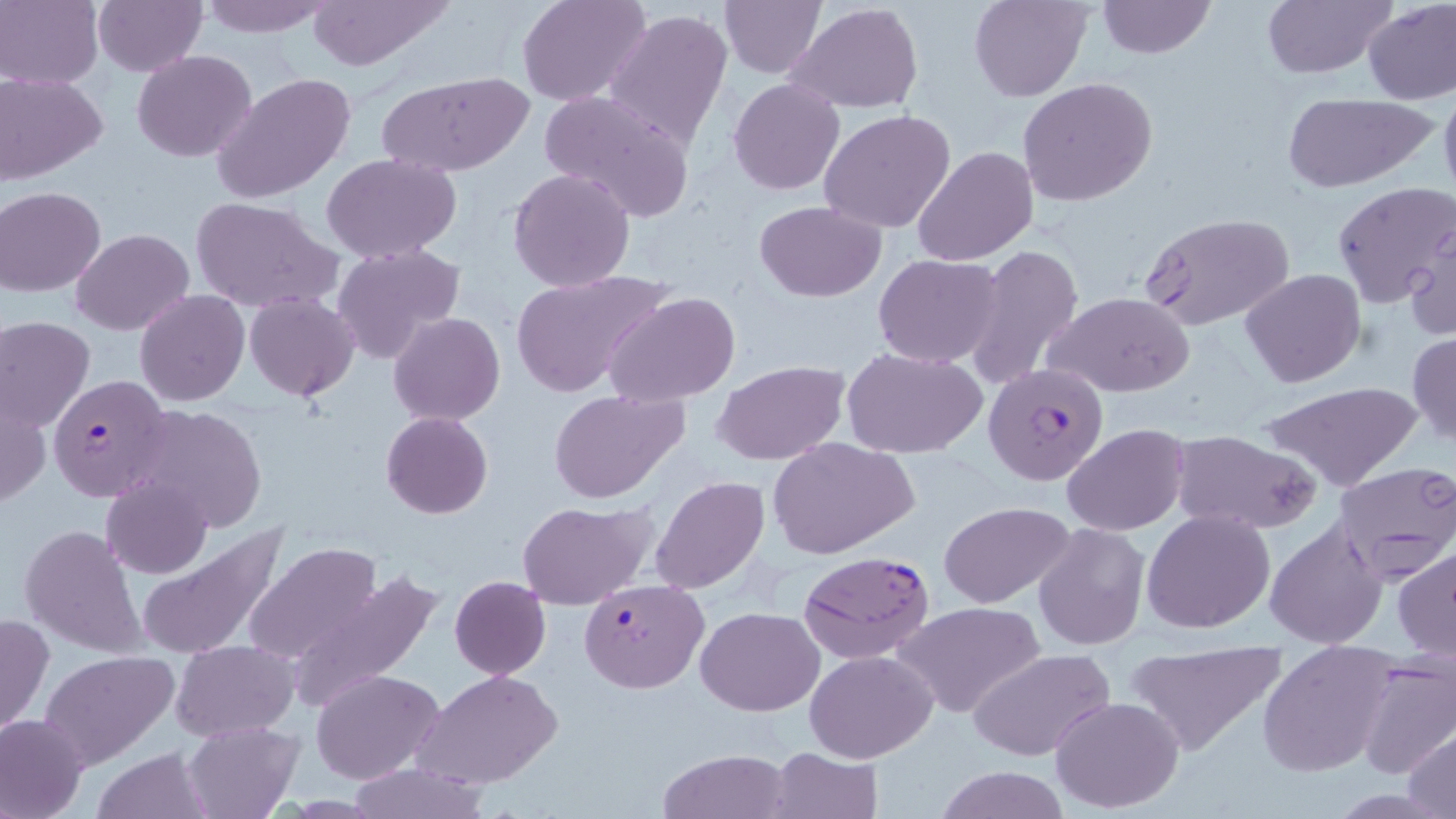

{
  "slide_level_diagnosis": "Plasmodium falciparum",
  "magnification": "1000x",
  "uninfected_red_blood_cell_locations": "approximate bounding boxes as named x1/y1/x2/y2 corners in pixels: (x1=92, y1=0, x2=207, y2=76), (x1=193, y1=0, x2=336, y2=38), (x1=304, y1=0, x2=452, y2=73), (x1=518, y1=0, x2=650, y2=107), (x1=718, y1=0, x2=825, y2=77), (x1=969, y1=0, x2=1090, y2=102), (x1=1097, y1=0, x2=1215, y2=59), (x1=1260, y1=0, x2=1395, y2=80), (x1=1362, y1=0, x2=1456, y2=105), (x1=0, y1=1, x2=102, y2=87), (x1=787, y1=2, x2=924, y2=114), (x1=602, y1=8, x2=733, y2=153), (x1=132, y1=50, x2=257, y2=162), (x1=379, y1=70, x2=533, y2=176), (x1=1, y1=72, x2=107, y2=184), (x1=211, y1=73, x2=357, y2=203), (x1=1438, y1=76, x2=1456, y2=204), (x1=1017, y1=77, x2=1158, y2=206), (x1=728, y1=79, x2=845, y2=195), (x1=540, y1=90, x2=696, y2=223), (x1=727, y1=91, x2=948, y2=210), (x1=1280, y1=92, x2=1435, y2=192), (x1=819, y1=109, x2=956, y2=234), (x1=914, y1=146, x2=1038, y2=265), (x1=320, y1=154, x2=461, y2=262), (x1=508, y1=167, x2=636, y2=292), (x1=1333, y1=181, x2=1455, y2=308), (x1=0, y1=187, x2=106, y2=296), (x1=192, y1=198, x2=340, y2=315), (x1=756, y1=201, x2=886, y2=301), (x1=1140, y1=213, x2=1295, y2=333), (x1=1404, y1=217, x2=1455, y2=343), (x1=72, y1=228, x2=193, y2=335), (x1=332, y1=242, x2=466, y2=367), (x1=963, y1=244, x2=1086, y2=389), (x1=873, y1=253, x2=1005, y2=368), (x1=511, y1=268, x2=671, y2=399), (x1=1240, y1=268, x2=1366, y2=386), (x1=135, y1=290, x2=248, y2=405), (x1=244, y1=291, x2=360, y2=402), (x1=606, y1=291, x2=740, y2=408), (x1=1047, y1=292, x2=1194, y2=397), (x1=389, y1=312, x2=506, y2=424), (x1=0, y1=318, x2=95, y2=433), (x1=1408, y1=331, x2=1456, y2=447), (x1=844, y1=348, x2=988, y2=459), (x1=712, y1=360, x2=848, y2=465), (x1=1258, y1=381, x2=1422, y2=492), (x1=547, y1=389, x2=690, y2=504), (x1=0, y1=392, x2=49, y2=509), (x1=129, y1=404, x2=269, y2=536), (x1=380, y1=411, x2=492, y2=519), (x1=1063, y1=424, x2=1187, y2=535), (x1=1170, y1=429, x2=1322, y2=534), (x1=766, y1=436, x2=919, y2=559), (x1=1331, y1=461, x2=1456, y2=581), (x1=650, y1=475, x2=770, y2=595), (x1=102, y1=476, x2=213, y2=579), (x1=517, y1=499, x2=655, y2=610), (x1=939, y1=501, x2=1076, y2=608), (x1=1143, y1=510, x2=1275, y2=631), (x1=1264, y1=519, x2=1386, y2=648), (x1=1031, y1=522, x2=1150, y2=652), (x1=20, y1=524, x2=146, y2=658), (x1=136, y1=525, x2=291, y2=661), (x1=244, y1=542, x2=385, y2=668), (x1=1392, y1=547, x2=1456, y2=663), (x1=287, y1=571, x2=443, y2=713), (x1=449, y1=575, x2=551, y2=679), (x1=896, y1=601, x2=1045, y2=718), (x1=697, y1=606, x2=823, y2=714), (x1=0, y1=612, x2=51, y2=740), (x1=1121, y1=638, x2=1291, y2=757), (x1=172, y1=640, x2=299, y2=740), (x1=1258, y1=640, x2=1398, y2=776), (x1=968, y1=647, x2=1115, y2=761), (x1=805, y1=648, x2=939, y2=763), (x1=38, y1=650, x2=180, y2=772), (x1=1352, y1=657, x2=1456, y2=781), (x1=311, y1=669, x2=444, y2=784), (x1=416, y1=671, x2=562, y2=790), (x1=1050, y1=696, x2=1184, y2=811), (x1=0, y1=714, x2=90, y2=817), (x1=182, y1=721, x2=301, y2=818), (x1=1407, y1=727, x2=1456, y2=816), (x1=766, y1=746, x2=884, y2=819), (x1=92, y1=747, x2=217, y2=818), (x1=659, y1=748, x2=791, y2=819), (x1=344, y1=763, x2=493, y2=819), (x1=931, y1=765, x2=1075, y2=819)",
  "modality": "light microscopy",
  "stain": "May-Grünwald-Giemsa",
  "field_of_view": "one of a larger specimen",
  "image_size": "1456×819 pixels",
  "plasmodium_falciparum_infected_red_blood_cell_locations": "approximate bounding boxes as named x1/y1/x2/y2 corners in pixels: (x1=983, y1=362, x2=1110, y2=487), (x1=48, y1=373, x2=172, y2=503), (x1=799, y1=550, x2=934, y2=662), (x1=579, y1=578, x2=708, y2=692)",
  "preparation": "thin blood film"
}